Outline each Plasmodium falciparum-infected red blood cell.
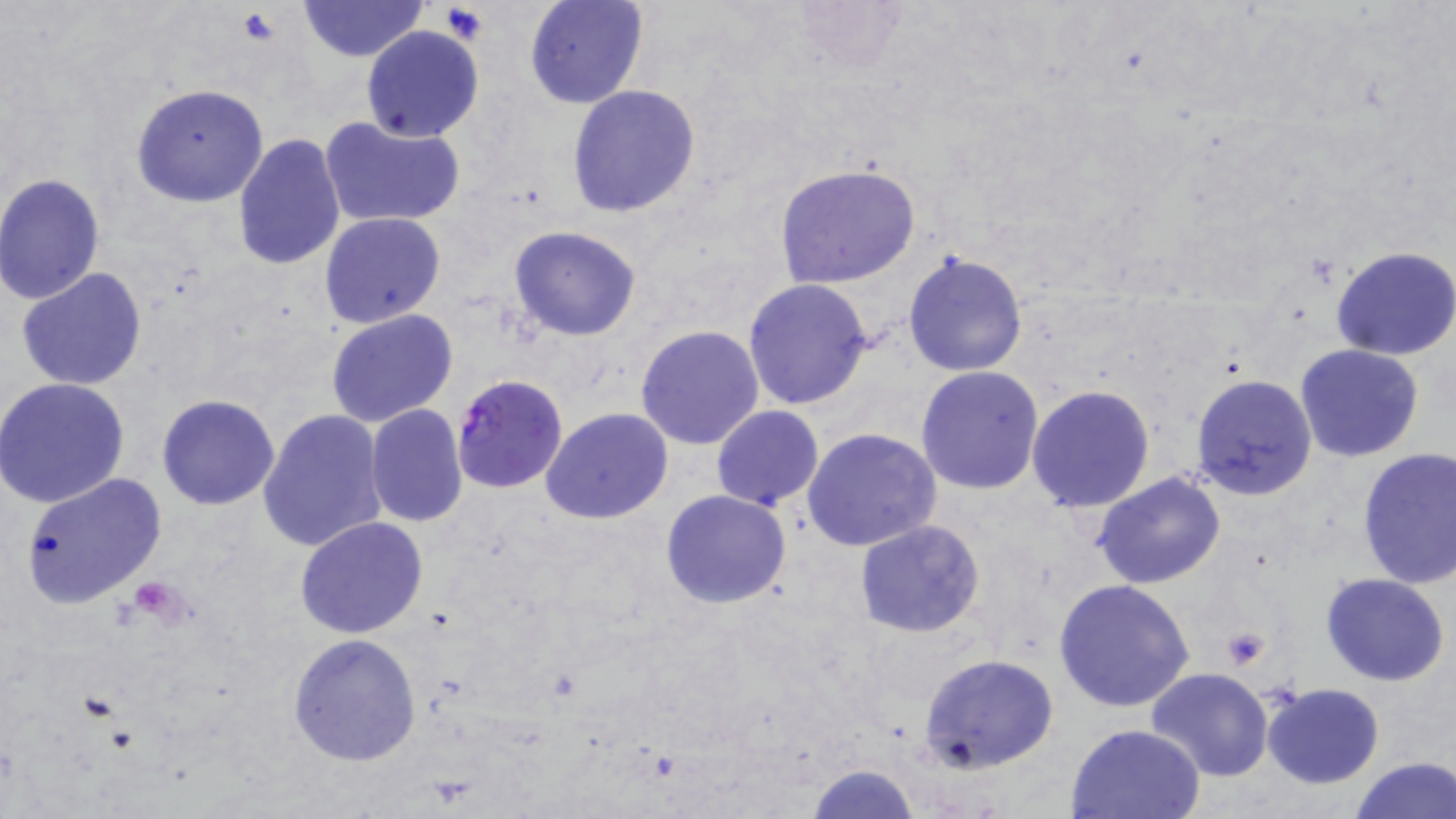

Approximate bounding boxes as (x1,y1)-(x2,y2) corner pairs in pixels.
Plasmodium falciparum-infected red blood cells: (447,384)-(566,505).

{
  "slide_level_diagnosis": "Plasmodium falciparum",
  "preparation": "thin blood smear",
  "platelet_locations": "approximate bounding boxes as (x1,y1)-(x2,y2) corner pairs in pixels: (441,4)-(489,43), (235,9)-(281,43), (131,581)-(188,621), (1219,628)-(1270,670)",
  "uninfected_red_blood_cell_locations": "approximate bounding boxes as (x1,y1)-(x2,y2) corner pairs in pixels: (298,0)-(427,61), (524,0)-(648,110), (785,0)-(908,75), (361,25)-(483,141), (132,84)-(269,208), (566,85)-(701,217), (319,116)-(465,228), (231,132)-(345,271), (773,164)-(921,289), (0,173)-(106,304), (320,212)-(448,329), (508,226)-(641,341), (1331,247)-(1456,361), (902,251)-(1030,377), (16,267)-(150,390), (744,279)-(875,411), (325,309)-(456,427), (635,324)-(765,449), (1294,342)-(1425,462), (915,366)-(1044,495), (1190,373)-(1318,502), (0,376)-(130,508), (1026,385)-(1156,514), (156,394)-(281,510), (365,405)-(469,527), (711,405)-(823,511), (541,408)-(674,525), (257,409)-(387,555), (803,428)-(942,553), (1355,446)-(1456,590), (19,472)-(168,607), (1092,473)-(1227,590), (660,490)-(792,610), (295,517)-(429,639), (854,519)-(986,638), (1320,571)-(1450,685), (1054,579)-(1195,712), (287,632)-(421,766), (919,653)-(1059,773), (1145,668)-(1275,782), (1261,682)-(1385,787), (1066,723)-(1209,818), (1348,756)-(1455,819), (805,763)-(921,818)",
  "magnification": "1000x",
  "modality": "light microscopy",
  "stain": "May-Grünwald-Giemsa",
  "field_of_view": "single",
  "image_size": "1456×819 pixels"
}